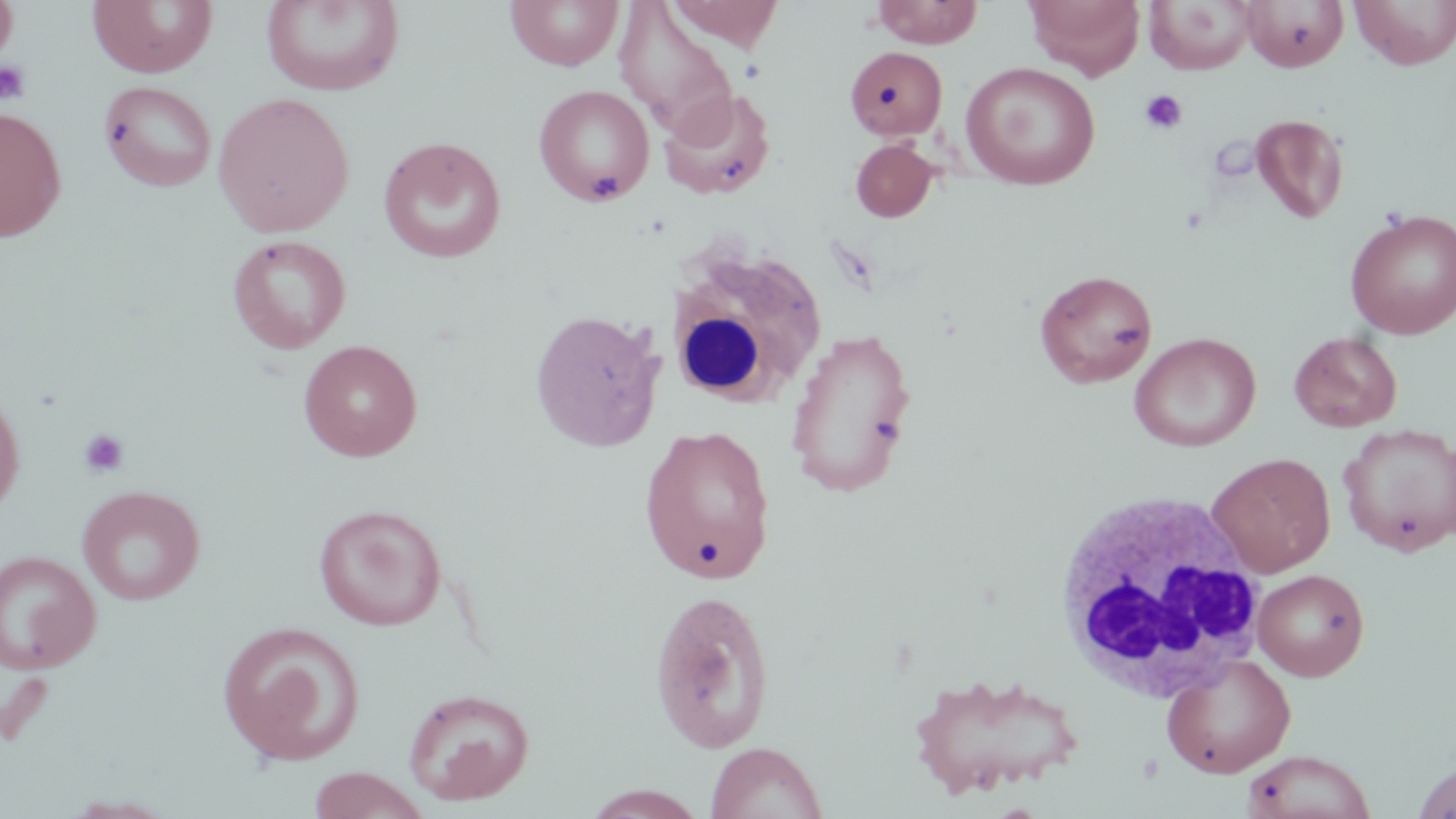

Summary:
  - Coordinate format: approximate bounding boxes as (x1, y1, x2, y2) in pixels
  - Platelet locations: (0, 59, 32, 106), (1139, 89, 1188, 134), (583, 167, 623, 203), (78, 428, 130, 478)
  - White blood cell locations: (666, 245, 828, 410), (1052, 489, 1271, 704)
  - Uninfected red blood cell locations: (505, 0, 624, 71), (871, 0, 983, 48), (1024, 0, 1145, 79), (1240, 0, 1349, 72), (1349, 0, 1456, 69), (0, 1, 19, 63), (86, 1, 219, 78), (261, 1, 404, 96), (666, 1, 784, 52), (1144, 1, 1254, 75), (614, 3, 736, 133), (845, 45, 948, 140), (960, 61, 1101, 191), (99, 80, 217, 192), (533, 84, 655, 207), (658, 88, 776, 200), (212, 91, 355, 237), (0, 107, 67, 242), (1249, 113, 1349, 224), (378, 136, 507, 264), (850, 139, 939, 222), (1344, 207, 1456, 339), (227, 235, 352, 354), (1034, 269, 1158, 389), (529, 308, 666, 452), (785, 327, 918, 498), (1129, 332, 1261, 452), (1289, 332, 1403, 432), (298, 339, 422, 462), (0, 380, 26, 521), (1338, 422, 1456, 557), (639, 424, 777, 584), (1207, 452, 1336, 577), (77, 485, 206, 606), (314, 504, 447, 631), (0, 549, 102, 674), (1252, 568, 1370, 681), (649, 589, 776, 753), (216, 621, 365, 765), (1161, 653, 1296, 778), (908, 669, 1083, 800), (402, 687, 535, 806), (705, 741, 828, 819), (1240, 749, 1377, 819), (1411, 761, 1456, 819), (305, 767, 433, 819), (579, 785, 709, 819)
  - Slide-level diagnosis: no evidence of blood parasites
  - Preparation: thin blood film
  - Stain: May-Grünwald-Giemsa
  - Magnification: 1000x
  - Modality: light microscopy
  - Field of view: single
  - Image size: 1456×819 pixels